Classify this cell by malaria status.
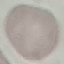
Uninfected.

Thin smear of blood. Automatically extracted cell patch, resized to 64 × 64 pixels. Photographed with a smartphone camera at the microscope eyepiece. Giemsa stain.